Report the malaria status of this cell.
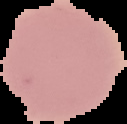

It is uninfected.

The area outside the segmented cell region is set to black. From a thin blood smear. Image is 127×124 pixels.